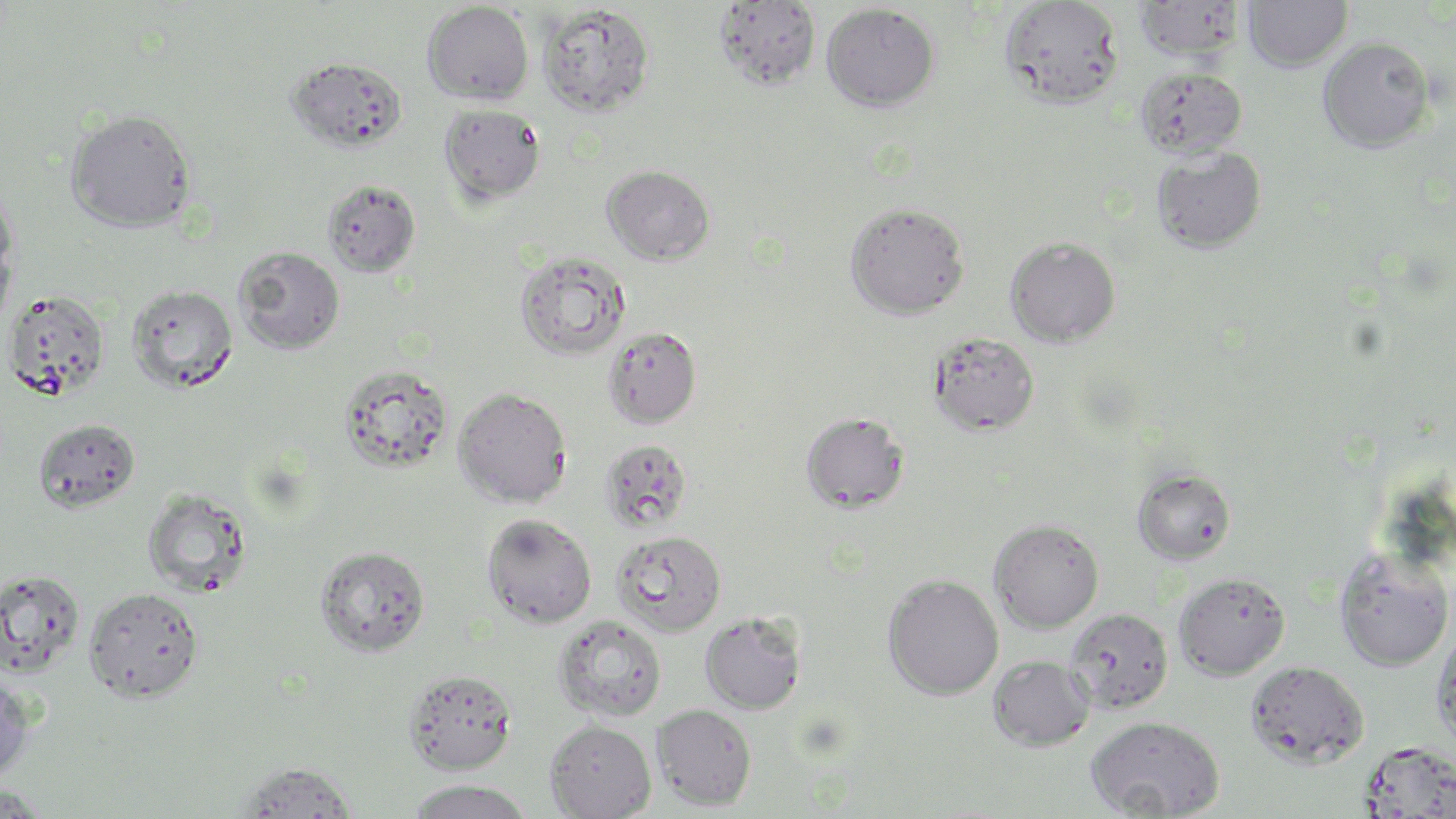
slide-level diagnosis = negative for blood parasites
preparation = thin blood film
uninfected red blood cell locations = approximate bounding boxes as [x1, y1, x2, y2] in pixels: [1134, 0, 1246, 62], [1242, 0, 1352, 71], [712, 1, 821, 93], [998, 1, 1124, 110], [422, 2, 534, 105], [820, 2, 940, 112], [536, 3, 655, 118], [1317, 37, 1436, 153], [284, 57, 409, 153], [1135, 66, 1246, 159], [438, 103, 546, 206], [64, 109, 196, 232], [1151, 145, 1267, 255], [601, 165, 716, 265], [322, 179, 422, 277], [0, 183, 18, 290], [844, 201, 970, 319], [0, 236, 16, 334], [1005, 236, 1121, 347], [233, 245, 346, 354], [513, 249, 631, 361], [126, 284, 239, 394], [3, 289, 111, 402], [602, 325, 701, 429], [929, 330, 1040, 436], [337, 364, 454, 474], [452, 387, 573, 508], [801, 411, 910, 514], [33, 418, 141, 513], [600, 438, 693, 533], [1132, 467, 1236, 564], [142, 487, 254, 597], [481, 514, 597, 628], [989, 518, 1104, 633], [610, 529, 727, 636], [315, 545, 431, 657], [1333, 548, 1454, 672], [0, 568, 85, 677], [1173, 572, 1290, 679], [882, 574, 1003, 700], [84, 586, 204, 702], [1065, 608, 1172, 713], [700, 611, 806, 715], [553, 614, 667, 723], [1432, 625, 1456, 751], [988, 654, 1095, 752], [1245, 660, 1369, 769], [403, 669, 517, 774], [0, 670, 35, 782], [651, 703, 757, 811], [1086, 715, 1225, 818], [545, 719, 656, 819], [1359, 740, 1456, 817], [234, 761, 360, 818], [405, 780, 536, 819], [0, 782, 53, 818]
stain = May-Grünwald-Giemsa
image size = 1456×819 pixels
magnification = 1000x
field of view = one of a larger specimen
modality = light microscopy